Locate every uninfected red blood cell.
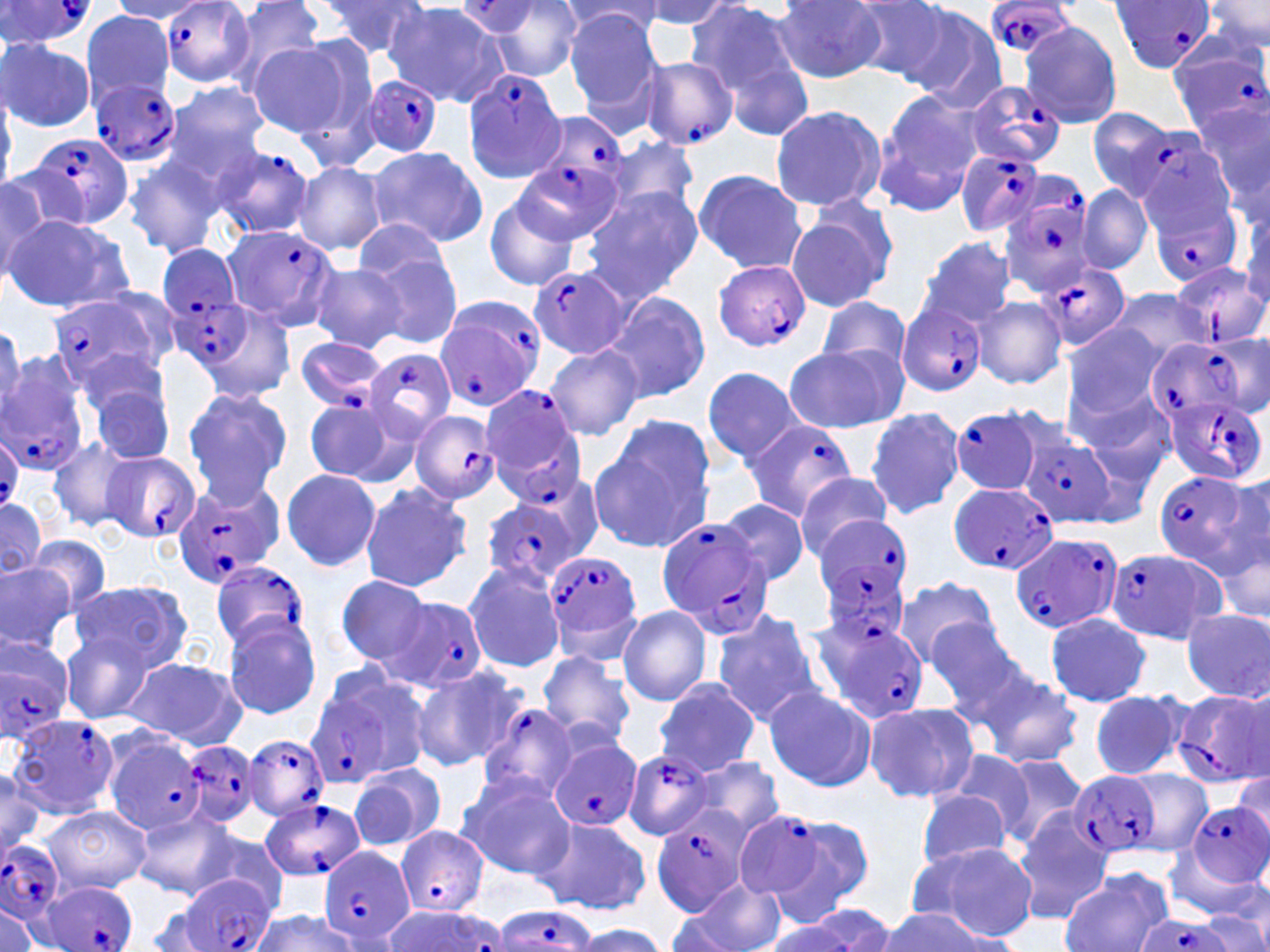
Approximate bounding boxes as (x1,y1)-(x2,y2) corner pairs in pixels.
Uninfected red blood cells: (220,0)-(329,90), (636,0)-(735,30), (685,0)-(808,122), (848,0)-(952,82), (1201,0)-(1270,55), (318,1)-(430,61), (774,1)-(887,82), (107,2)-(211,23), (385,2)-(511,107), (473,2)-(585,81), (560,2)-(667,41), (901,4)-(1008,111), (81,10)-(175,106), (563,10)-(664,115), (1019,20)-(1122,128), (0,38)-(94,131), (246,41)-(355,138), (286,41)-(381,164), (166,81)-(270,176), (872,89)-(984,213), (1194,100)-(1268,202), (769,105)-(886,210), (1086,109)-(1178,201), (604,135)-(699,215), (365,146)-(488,249), (125,152)-(224,259), (292,161)-(386,256), (692,169)-(806,275), (0,173)-(53,280), (1075,183)-(1152,276), (581,187)-(703,298), (483,193)-(581,290), (1239,200)-(1269,310), (786,205)-(895,311), (4,215)-(133,313), (355,220)-(453,297), (917,237)-(1019,328), (361,248)-(463,351), (309,262)-(409,354), (1108,288)-(1211,368), (601,291)-(710,403), (817,296)-(912,372), (974,296)-(1066,388), (1062,322)-(1169,423), (1209,332)-(1269,416), (545,341)-(642,439), (784,344)-(904,433), (77,351)-(169,424), (701,366)-(802,465), (89,379)-(177,466), (1070,382)-(1177,483), (182,386)-(291,503), (302,396)-(415,487), (864,408)-(965,519), (588,418)-(716,553), (47,436)-(138,533), (281,469)-(381,571), (792,473)-(896,561), (1213,473)-(1270,576), (359,482)-(475,592), (0,497)-(48,579), (718,498)-(811,588), (1214,526)-(1270,633), (27,534)-(113,619), (0,561)-(75,656), (464,561)-(568,672), (335,575)-(434,668), (892,575)-(999,670), (70,580)-(192,674), (618,605)-(712,706), (710,608)-(826,724), (1181,608)-(1269,702), (1045,612)-(1151,707), (223,615)-(322,720), (925,620)-(1030,722), (59,630)-(157,724), (535,650)-(637,753), (123,656)-(244,746), (969,663)-(1083,769), (410,664)-(526,771), (652,677)-(762,777), (762,685)-(876,793), (1088,691)-(1189,779), (865,700)-(981,804), (983,751)-(1091,848), (947,752)-(1036,839), (695,756)-(785,842), (349,763)-(445,851), (0,764)-(44,857), (1122,768)-(1210,856), (1231,773)-(1269,844), (457,774)-(574,878), (912,789)-(1015,875), (479,796)-(624,909), (38,804)-(151,895), (1012,807)-(1115,925), (132,809)-(237,898), (766,813)-(877,912), (536,814)-(652,916), (192,828)-(290,916), (911,840)-(1037,939), (1060,868)-(1171,952), (681,876)-(786,952), (0,901)-(45,949), (141,904)-(228,951), (664,904)-(752,951), (782,904)-(897,951), (879,906)-(1004,950), (1198,909)-(1269,952), (248,911)-(357,952), (570,923)-(668,952).

slide-level diagnosis = Plasmodium falciparum
image size = 1270×952 pixels
stain = May-Grünwald-Giemsa
preparation = thin blood film
Plasmodium falciparum-infected red blood cell locations = approximate bounding boxes as (x1,y1)-(x2,y2) corner pairs in pixels: (156,0)-(269,90), (982,0)-(1077,58), (1112,0)-(1216,74), (0,1)-(98,47), (1168,35)-(1267,133), (639,57)-(739,150), (463,67)-(568,184), (363,74)-(444,157), (87,79)-(183,169), (964,81)-(1064,169), (530,115)-(623,213), (1131,131)-(1237,234), (25,136)-(134,230), (212,145)-(316,239), (954,149)-(1050,237), (517,157)-(623,247), (1146,185)-(1247,287), (996,187)-(1097,296), (221,224)-(338,331), (147,243)-(241,327), (713,259)-(812,353), (1172,260)-(1267,349), (1040,261)-(1132,351), (531,265)-(629,359), (47,292)-(166,394), (170,294)-(255,371), (433,297)-(542,411), (898,303)-(988,396), (294,337)-(389,412), (1150,338)-(1248,427), (364,350)-(456,438), (0,360)-(89,477), (478,384)-(586,503), (1164,393)-(1263,486), (948,407)-(1047,494), (407,408)-(501,504), (741,416)-(857,521), (0,428)-(21,512), (1023,435)-(1116,527), (99,450)-(200,545), (1152,470)-(1253,567), (173,478)-(284,588), (947,480)-(1057,575), (482,498)-(580,589), (655,517)-(773,639), (815,520)-(914,608), (1010,532)-(1121,636), (1105,548)-(1226,643), (544,550)-(642,656), (211,562)-(311,651), (386,597)-(487,692), (812,615)-(927,722), (0,638)-(75,740), (1171,687)-(1268,785), (303,691)-(395,787), (478,706)-(578,799), (9,716)-(121,817), (244,734)-(328,821), (107,737)-(207,835), (178,737)-(263,831), (549,740)-(642,833), (623,748)-(713,839), (1071,771)-(1161,860), (259,797)-(366,882), (1188,802)-(1270,886), (732,811)-(833,903), (649,816)-(748,916), (394,826)-(489,918), (0,838)-(66,924), (318,845)-(416,949), (179,875)-(276,952), (36,881)-(139,952), (490,907)-(599,951), (1134,915)-(1229,952)
magnification = 1000x
modality = light microscopy
field of view = one of a larger specimen